Assess this cell for malaria.
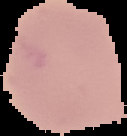
Uninfected.

{
  "image_size": "127×136 pixels",
  "image_type": "segmented cell region with the area outside set to black",
  "preparation": "thin blood smear"
}